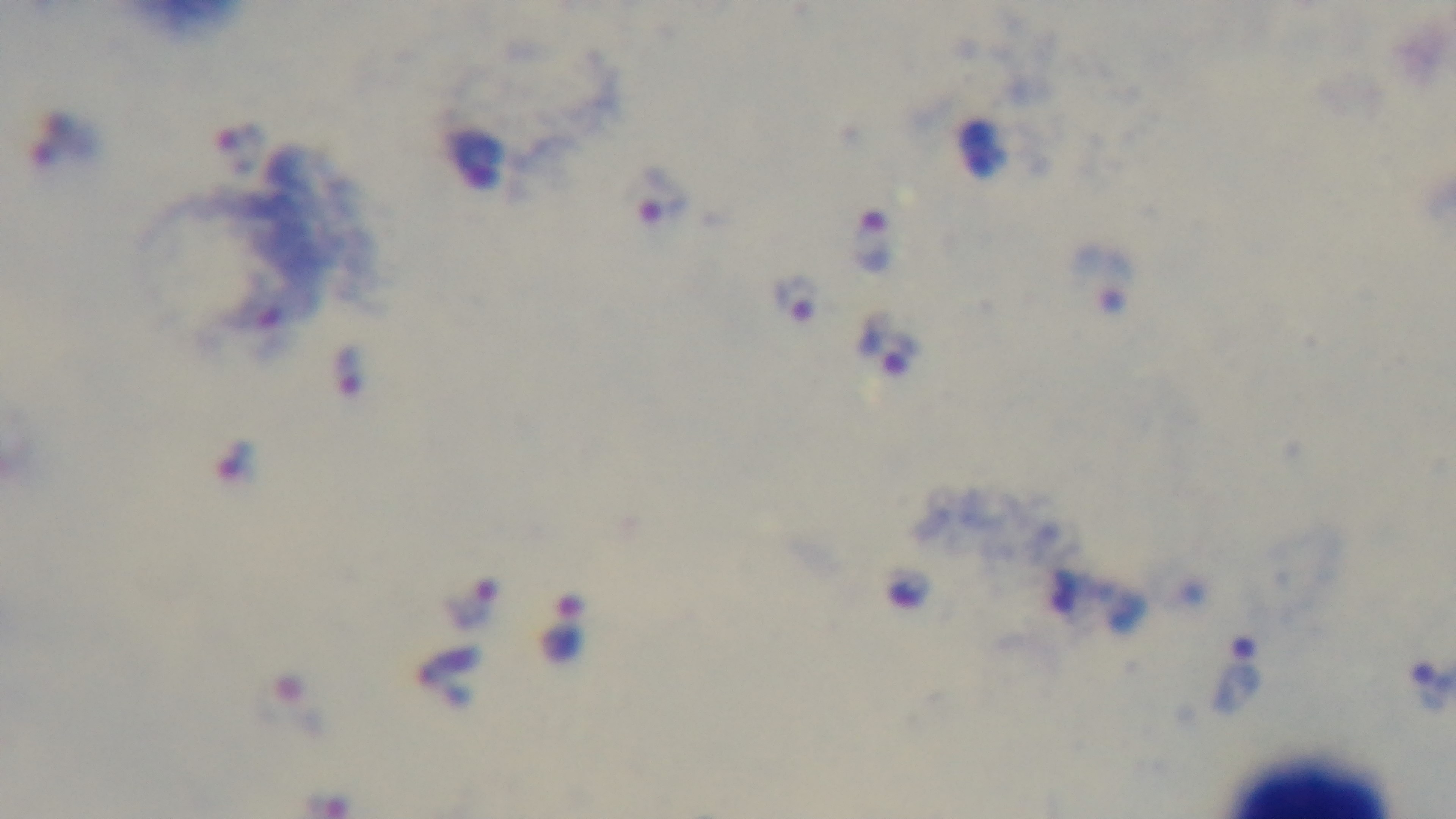

Summary:
  - Field of view: one from the slide
  - Malaria status: positive
  - Capture: mounted 4K digital camera
  - Preparation: thick
  - Objective: 100x oil immersion
  - Stain: Giemsa
  - Modality: light microscopy